Report the malaria status of this cell.
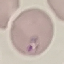
It is parasitized.

Thin smear of blood. Giemsa stain. Photographed with a smartphone camera at the microscope eyepiece. Automatically extracted cell patch, resized to 64 × 64 pixels.